Identify the parasite.
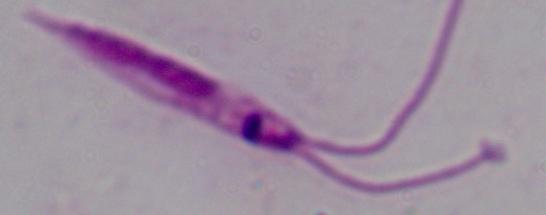
Leishmania.

modality = micrograph
magnification = 1000x